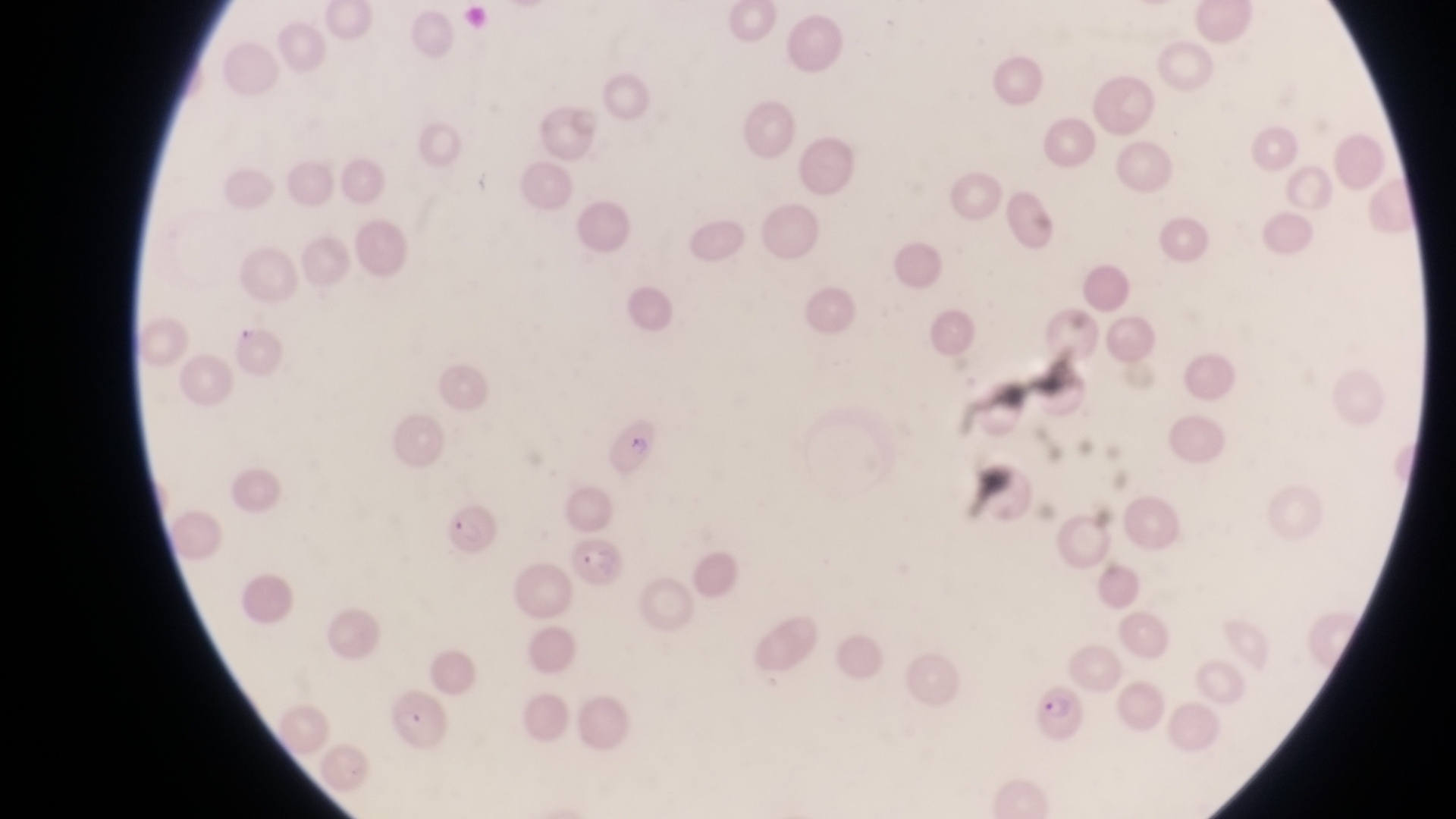 Approximate bounding boxes as left top right bottom in pixels. Parasitised red blood cell locations: 598 412 657 470; 439 507 502 557; 563 536 622 595; 1028 682 1087 743; 383 689 456 753. One field of view. At a magnification of 1000x. Thin blood film. Image is 1456×819 pixels. Captured by a smartphone held over the eyepiece of an Olympus CX-23 microscope. Collected in Uganda.